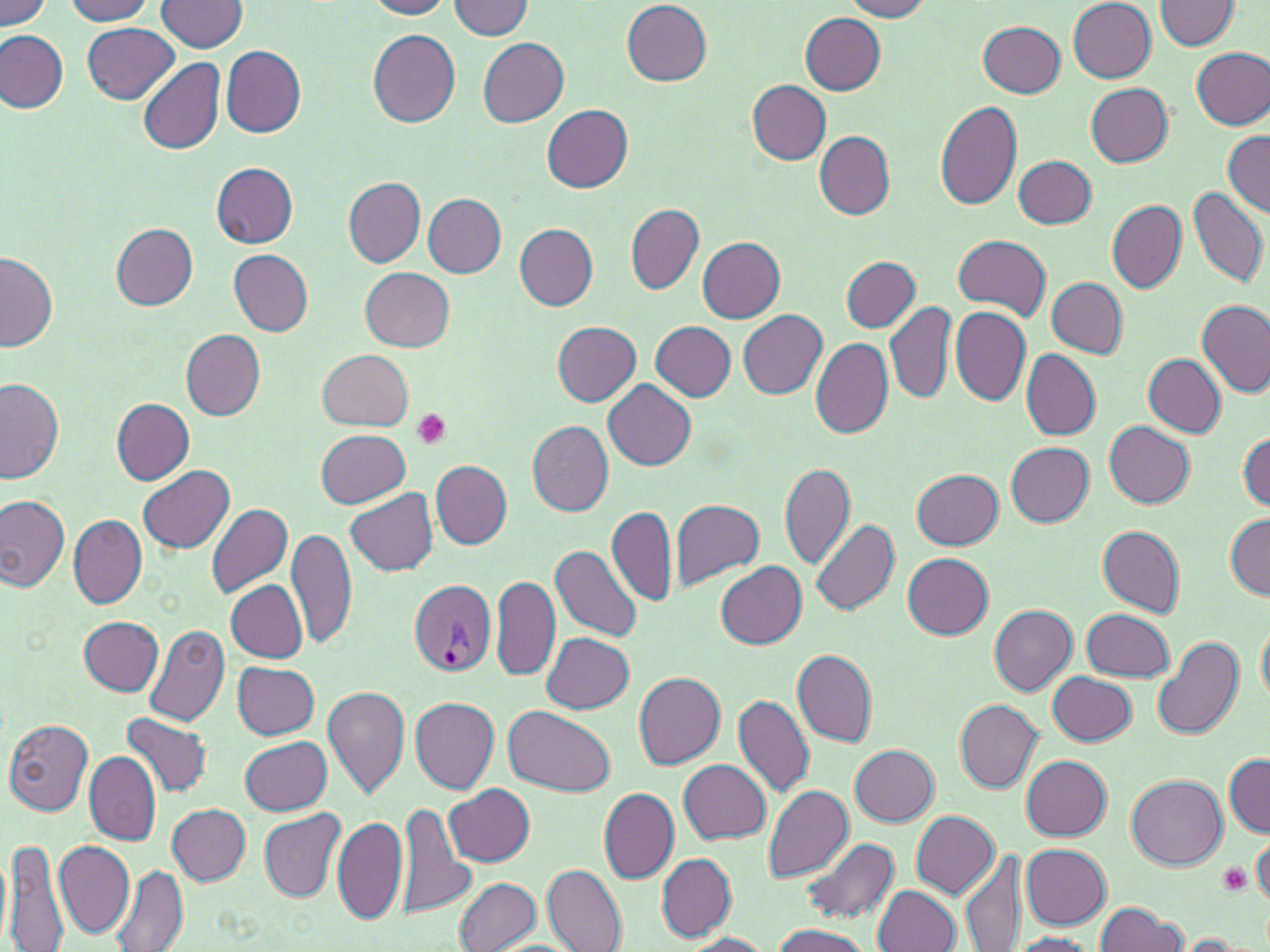

slide-level diagnosis = Plasmodium vivax
platelet locations = approximate bounding boxes as [x1, y1, x2, y2] in pixels: [410, 410, 452, 451], [1218, 862, 1251, 894]
uninfected red blood cell locations = approximate bounding boxes as [x1, y1, x2, y2] in pixels: [1, 0, 52, 28], [64, 0, 154, 23], [158, 0, 249, 52], [364, 0, 454, 19], [448, 0, 533, 38], [841, 0, 932, 21], [1068, 0, 1158, 83], [1152, 1, 1241, 51], [621, 2, 712, 85], [800, 13, 886, 94], [977, 19, 1066, 97], [83, 23, 180, 104], [369, 29, 462, 127], [0, 30, 69, 114], [478, 38, 569, 126], [220, 45, 305, 137], [1192, 47, 1270, 130], [138, 57, 225, 156], [746, 81, 830, 164], [1085, 82, 1174, 165], [934, 98, 1023, 209], [542, 105, 633, 192], [1221, 130, 1270, 215], [814, 132, 895, 220], [1013, 155, 1097, 227], [212, 163, 298, 247], [343, 177, 425, 265], [1188, 188, 1269, 287], [423, 194, 507, 276], [1106, 201, 1186, 292], [625, 204, 703, 293], [515, 223, 598, 310], [112, 224, 197, 308], [952, 236, 1051, 318], [697, 238, 785, 322], [229, 249, 313, 336], [1, 254, 58, 352], [843, 256, 919, 332], [360, 267, 454, 352], [1047, 278, 1128, 357], [1196, 299, 1270, 400], [885, 302, 954, 405], [950, 306, 1032, 407], [738, 310, 827, 398], [551, 320, 642, 406], [650, 321, 736, 401], [182, 331, 266, 420], [810, 338, 893, 439], [1021, 348, 1101, 440], [318, 349, 414, 431], [1142, 353, 1225, 437], [602, 379, 697, 468], [1, 380, 65, 484], [112, 399, 194, 484], [526, 420, 614, 516], [1105, 422, 1196, 509], [315, 429, 411, 507], [1238, 431, 1270, 511], [1006, 442, 1095, 526], [431, 459, 511, 548], [780, 463, 855, 568], [138, 465, 234, 553], [912, 469, 1003, 549], [345, 488, 438, 577], [0, 496, 70, 591], [671, 500, 764, 589], [206, 502, 294, 600], [606, 506, 676, 605], [68, 513, 147, 609], [1224, 513, 1270, 600], [811, 520, 899, 617], [1098, 525, 1187, 618], [287, 527, 357, 651], [550, 544, 642, 642], [902, 553, 993, 639], [717, 562, 806, 648], [491, 575, 561, 681], [226, 581, 308, 663], [989, 605, 1076, 695], [1083, 609, 1176, 681], [1257, 615, 1270, 708], [80, 616, 163, 695], [144, 624, 231, 727], [542, 632, 634, 714], [1153, 636, 1244, 741], [792, 649, 877, 747], [232, 662, 320, 738], [633, 671, 726, 768], [1048, 672, 1137, 745], [323, 684, 410, 799], [732, 695, 814, 799], [410, 696, 500, 792], [955, 700, 1043, 792], [504, 704, 615, 796], [121, 713, 214, 798], [4, 719, 95, 815], [241, 736, 332, 815], [851, 745, 939, 827], [84, 751, 161, 846], [1224, 753, 1270, 838], [1022, 755, 1111, 840], [679, 758, 771, 844], [1125, 775, 1226, 869], [762, 784, 853, 880], [445, 785, 535, 866], [599, 788, 680, 883], [397, 802, 472, 918], [169, 804, 249, 885], [259, 809, 345, 903], [911, 810, 1000, 898], [334, 815, 407, 925], [1251, 834, 1270, 908], [799, 836, 899, 925], [4, 838, 70, 951], [55, 839, 136, 939], [1021, 844, 1113, 927], [959, 849, 1026, 951], [657, 853, 736, 940], [542, 864, 626, 952], [111, 866, 190, 951], [454, 876, 543, 951], [873, 885, 961, 951], [1094, 903, 1188, 952], [768, 925, 873, 952], [679, 932, 774, 951], [1007, 933, 1102, 952], [1174, 934, 1263, 951]
image size = 1270×952 pixels
Plasmodium vivax-infected red blood cell locations = approximate bounding boxes as [x1, y1, x2, y2] in pixels: [408, 577, 497, 678]
field of view = single
modality = light microscopy
stain = May-Grünwald-Giemsa
preparation = thin blood smear
magnification = 1000x